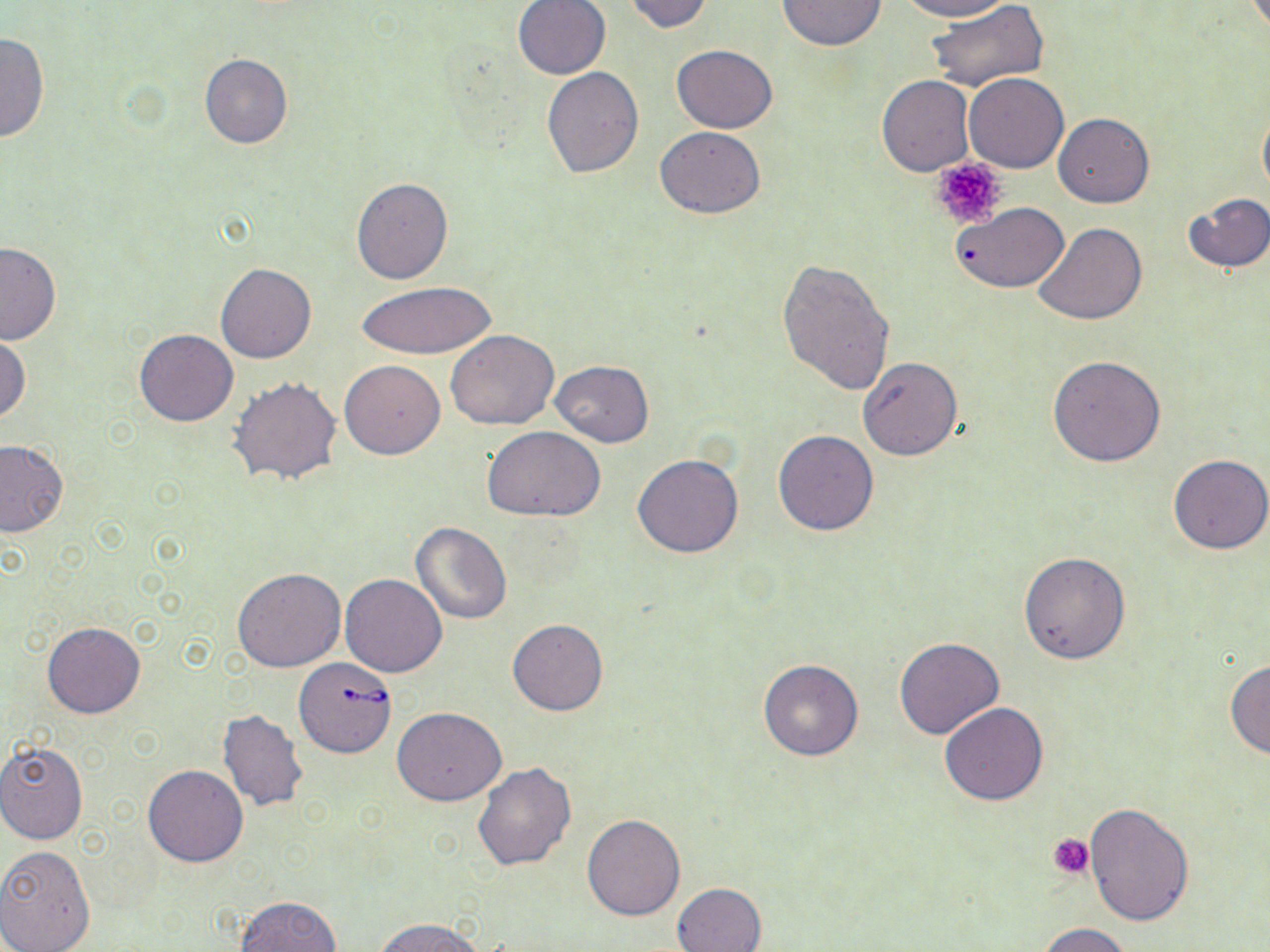

Summary:
  - Coordinate format: approximate bounding boxes as (x1, y1, x2, y2) in pixels
  - Platelet locations: (930, 155, 1010, 230), (1048, 832, 1094, 878)
  - Uninfected red blood cell locations: (512, 0, 610, 80), (624, 0, 714, 34), (777, 0, 889, 50), (899, 0, 1014, 22), (928, 1, 1051, 93), (0, 33, 48, 144), (671, 44, 777, 133), (198, 52, 293, 149), (541, 68, 644, 177), (962, 73, 1069, 173), (878, 75, 974, 175), (1258, 105, 1270, 201), (1054, 112, 1154, 207), (654, 126, 766, 217), (350, 177, 453, 284), (1182, 193, 1270, 274), (951, 203, 1069, 293), (1033, 223, 1148, 326), (0, 242, 62, 346), (777, 259, 895, 394), (216, 263, 315, 363), (355, 282, 497, 358), (133, 328, 238, 426), (446, 329, 559, 429), (0, 331, 30, 426), (1048, 354, 1166, 466), (858, 357, 962, 461), (339, 360, 445, 459), (550, 361, 655, 448), (228, 375, 342, 487), (482, 425, 606, 521), (772, 429, 879, 534), (0, 440, 68, 537), (632, 454, 743, 558), (1168, 454, 1270, 554), (411, 522, 512, 624), (1019, 552, 1130, 663), (232, 567, 345, 671), (341, 574, 446, 677), (507, 619, 608, 715), (41, 620, 146, 719), (894, 637, 1004, 739), (1225, 658, 1270, 758), (757, 659, 865, 760), (940, 702, 1050, 805), (392, 707, 506, 806), (217, 709, 309, 812), (0, 742, 88, 844), (472, 762, 577, 872), (143, 765, 247, 867), (1082, 801, 1194, 927), (581, 813, 685, 921), (0, 845, 96, 951), (672, 881, 767, 952), (235, 895, 343, 951), (376, 917, 485, 952), (1036, 922, 1135, 952)
  - Babesia divergens-infected red blood cell locations: (293, 661, 397, 758)
  - Slide-level diagnosis: Babesia divergens
  - Image size: 1270×952 pixels
  - Field of view: one of a larger specimen
  - Stain: May-Grünwald-Giemsa
  - Magnification: 1000x
  - Preparation: thin blood smear
  - Modality: light microscopy